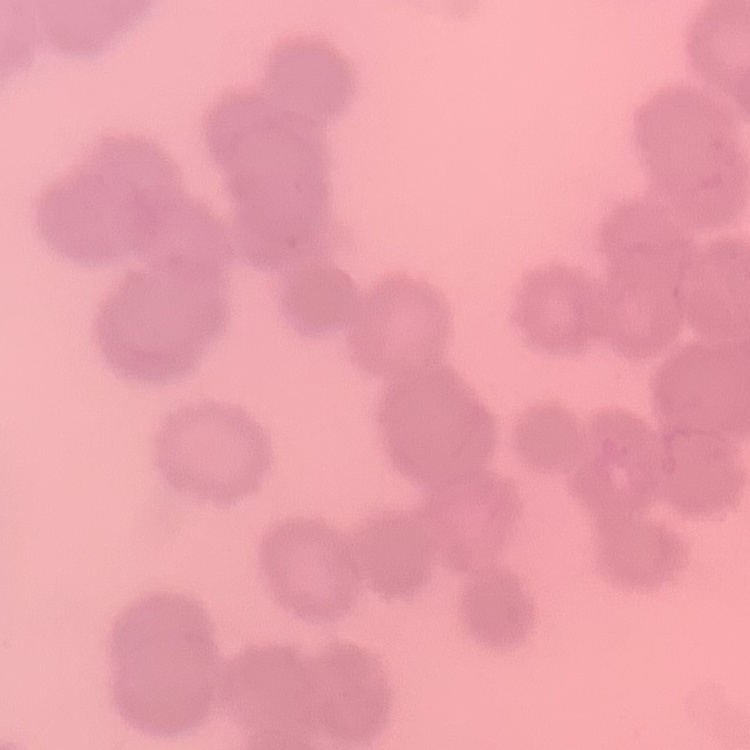
The red blood cells show rouleaux formation. Stained with either Field's or Giemsa. One tile cut from a larger photomicrograph. Thin blood film.